Identify the parasite.
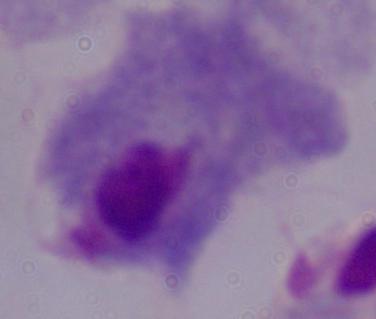

This is a trichomonad.

Summary:
  - Modality: photomicrograph
  - Magnification: 1000x